Assess this cell for malaria.
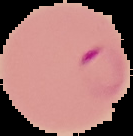
It is parasitized.

The area outside the segmented cell region is set to black. From a thin blood film. Image is 133×136 pixels.